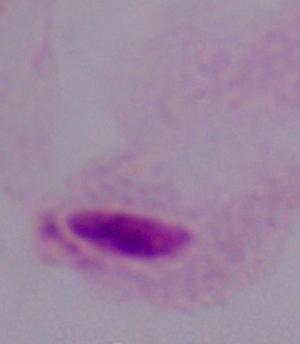

1000x magnification. A trichomonad is seen. Micrograph.